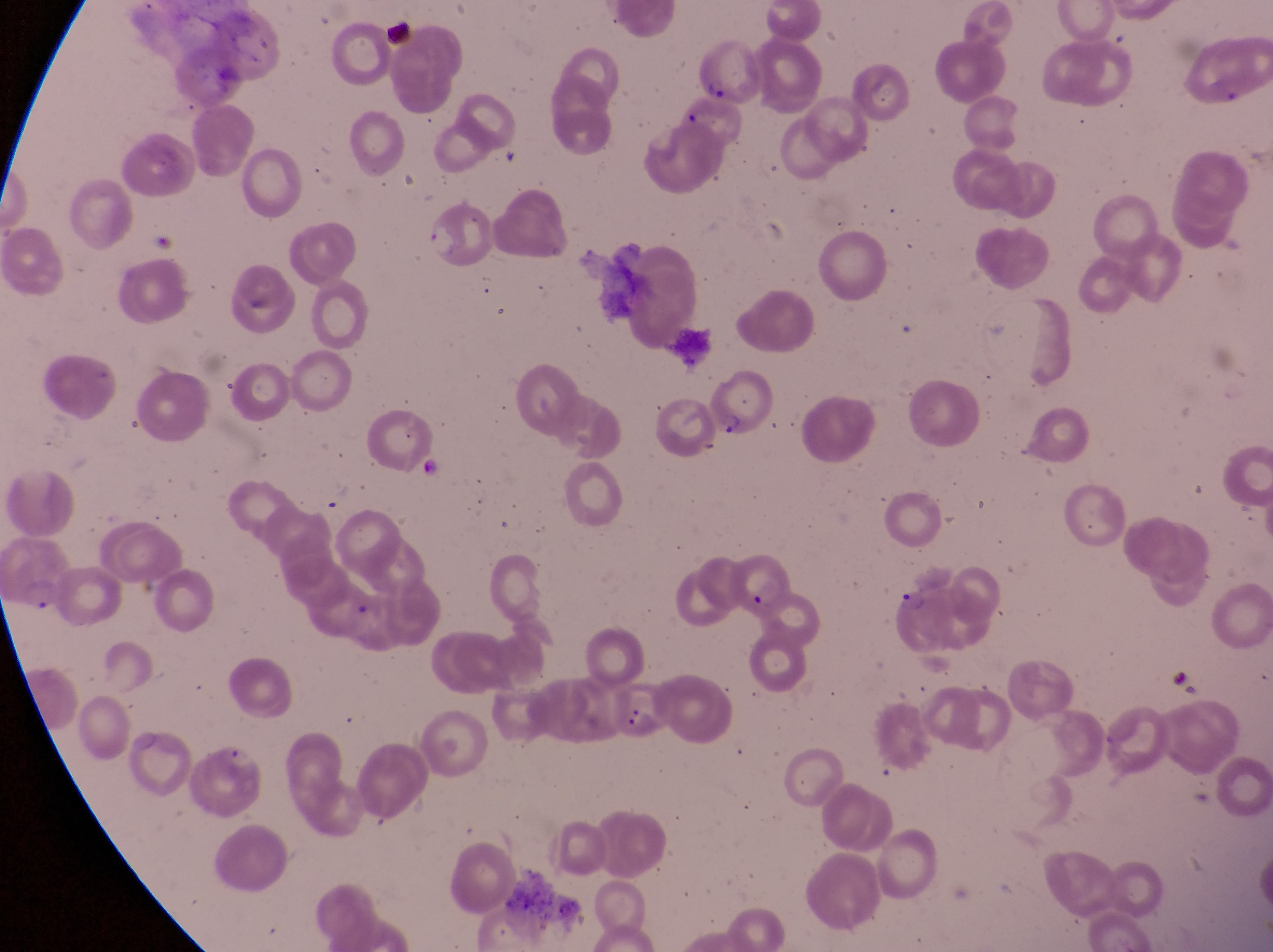
Approximate bounding boxes as left top right bottom in pixels.
Summary:
  - Parasitised red blood cell locations: 696 39 754 106; 677 98 746 161; 708 367 770 438; 8 534 77 619; 727 554 790 616; 884 580 953 655; 609 689 676 754
  - Artifact (platelet-like body, stain precipitate, or debris) locations: 380 10 419 52
  - Capture: smartphone photograph through the eyepiece of an Olympus CX-23 microscope
  - Preparation: thin blood film
  - Field of view: single
  - Magnification: 1000x
  - Image size: 1273×952 pixels
  - Country: Uganda